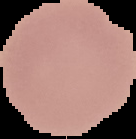
Summary:
  - Image size: 136×139 pixels
  - Image type: cell region segmented out of the field of view; surrounding area masked to black
  - Preparation: thin blood film
  - Malaria status: uninfected